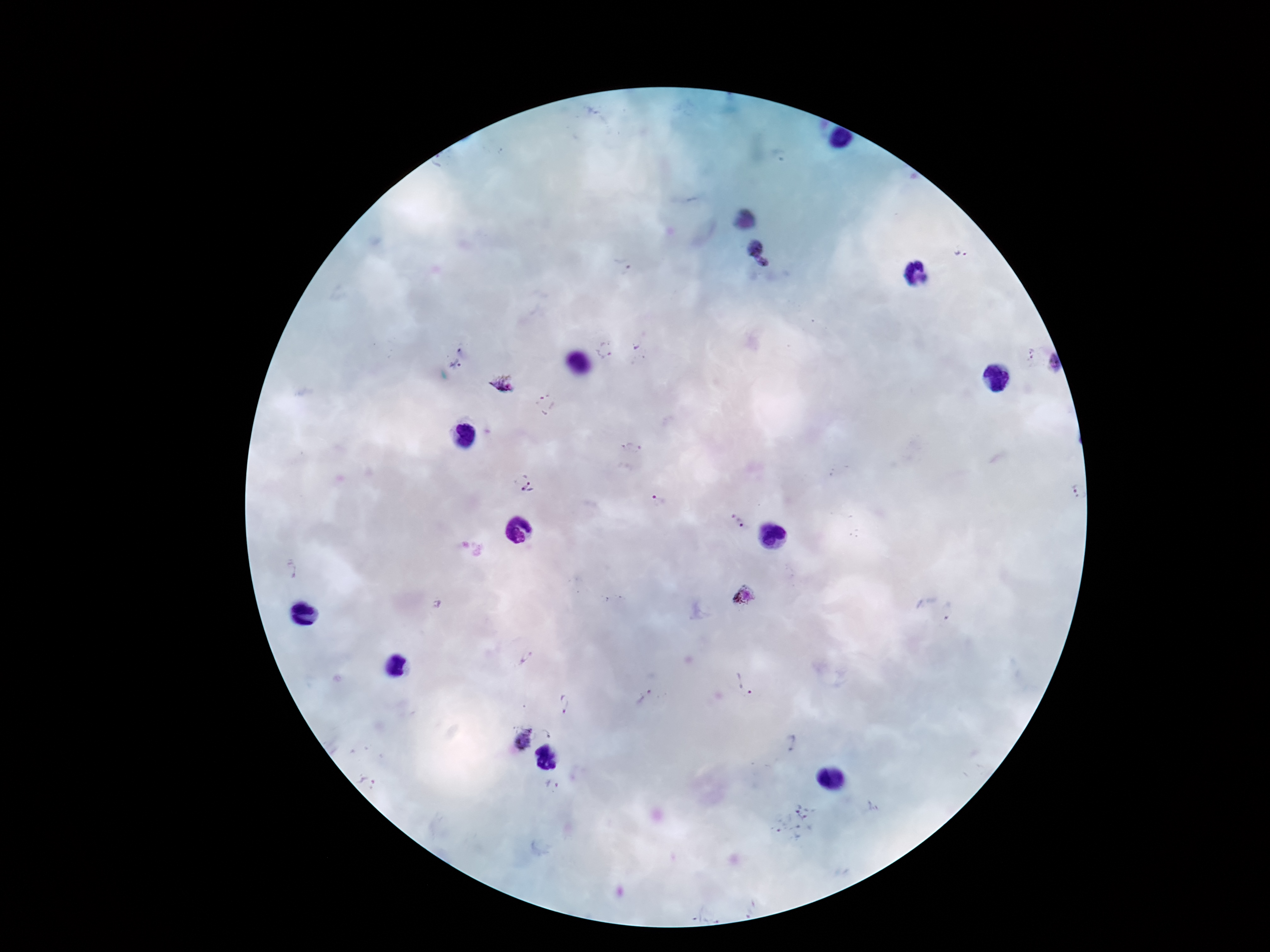

Approximate object centers, in pixels from the top-left corner. Plasmodium parasite locations: (x=756, y=248), (x=960, y=254), (x=764, y=264), (x=621, y=267), (x=604, y=350), (x=639, y=351), (x=455, y=365), (x=503, y=384), (x=546, y=405), (x=526, y=485), (x=657, y=502), (x=737, y=520), (x=291, y=570), (x=745, y=596), (x=437, y=604), (x=950, y=611), (x=527, y=658), (x=745, y=682), (x=643, y=697), (x=565, y=703), (x=548, y=731), (x=520, y=737), (x=791, y=743), (x=367, y=780), (x=552, y=784), (x=795, y=824). Photographed through the microscope eyepiece with a smartphone camera. Image is 1270×952 pixels. Thick blood film. 100x magnification. One field from this slide. Giemsa-stained preparation. Patient malaria status: infected.